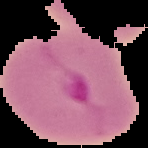 Image is 148×148 pixels. Cell region segmented out of the field of view; the surrounding area is masked to black. Result: malaria parasites identified. From a thin blood smear.